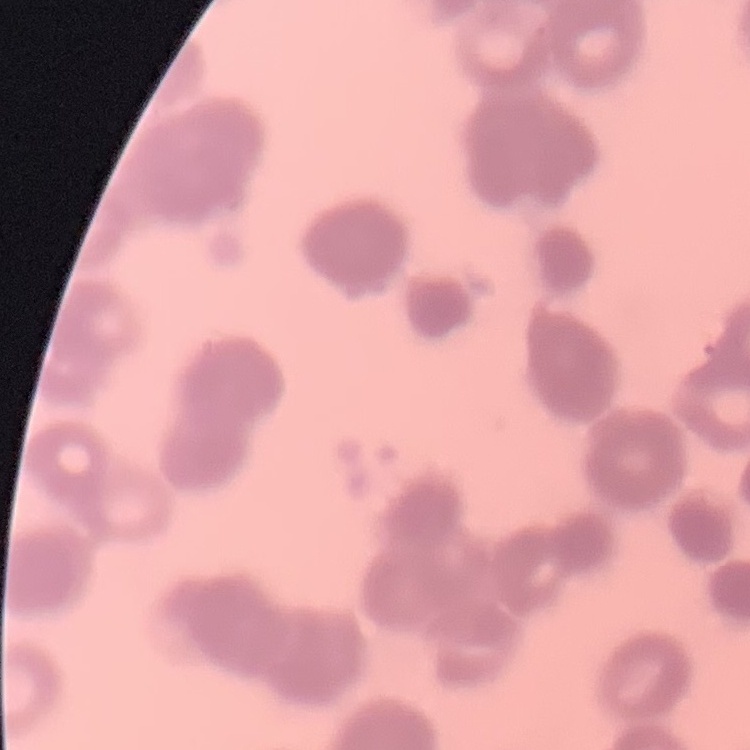

The erythrocytes show rouleaux formation. Field's or Giemsa stain. One tile cut from a larger photomicrograph. Thin peripheral smear.